Identify the blood parasite species.
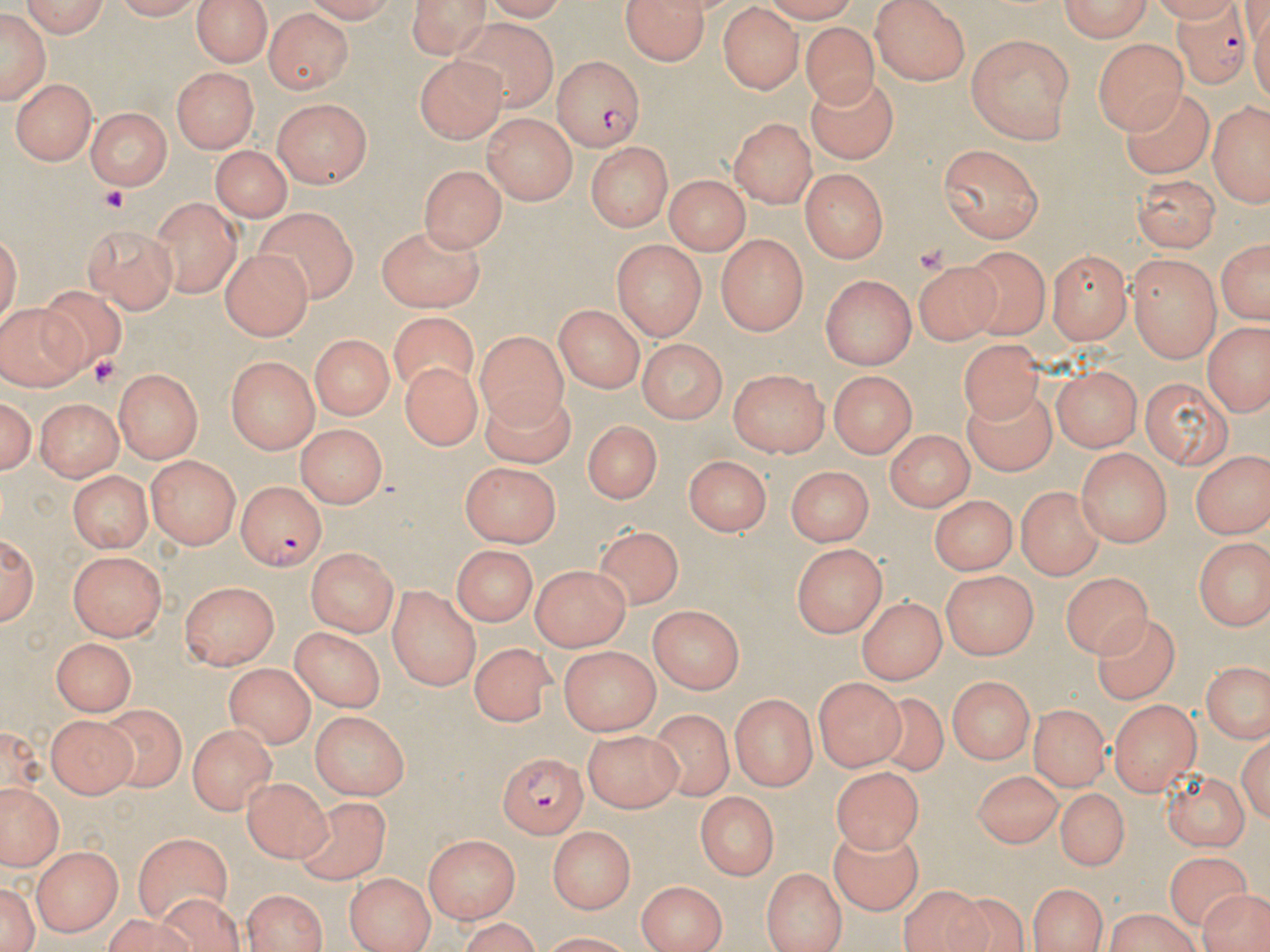
Plasmodium falciparum.

Approximate bounding boxes as (x1,y1)-(x2,y2) corner pairs in pixels. Platelet locations: (99,188)-(128,213), (86,355)-(122,389). Plasmodium falciparum-infected red blood cell locations: (1171,0)-(1251,91), (552,56)-(644,153), (233,480)-(324,569), (493,751)-(591,838). Uninfected red blood cell locations: (17,0)-(113,36), (105,0)-(200,21), (191,0)-(274,66), (403,0)-(494,56), (619,0)-(711,62), (1052,0)-(1152,40), (869,1)-(975,84), (0,6)-(46,107), (263,7)-(351,92), (717,8)-(801,94), (445,20)-(558,114), (802,22)-(877,106), (967,34)-(1076,144), (1093,37)-(1185,131), (417,56)-(507,143), (168,65)-(261,152), (807,76)-(896,164), (14,78)-(97,163), (1119,88)-(1214,180), (269,97)-(373,185), (1207,99)-(1270,207), (85,108)-(171,191), (481,112)-(578,203), (728,117)-(817,207), (587,141)-(674,230), (939,144)-(1045,244), (212,145)-(292,221), (420,164)-(508,255), (800,169)-(887,262), (1133,174)-(1220,254), (663,175)-(747,254), (150,196)-(243,296), (253,208)-(358,299), (1,221)-(22,334), (82,222)-(180,312), (374,223)-(488,310), (716,234)-(806,334), (1214,234)-(1268,330), (613,241)-(703,339), (963,243)-(1050,344), (1050,249)-(1130,346), (221,251)-(311,341), (1127,257)-(1222,364), (911,258)-(1001,343), (821,276)-(916,369), (34,288)-(127,371), (1,301)-(85,390), (555,303)-(647,393), (390,310)-(476,391), (1204,321)-(1269,417), (479,328)-(569,423), (308,335)-(391,421), (636,339)-(731,421), (960,342)-(1042,429), (227,358)-(321,452), (399,361)-(485,451), (730,366)-(831,455), (1052,366)-(1143,450), (114,368)-(204,462), (831,371)-(917,458), (1142,373)-(1234,466), (478,386)-(577,467), (959,386)-(1059,480), (0,390)-(38,483), (37,398)-(121,481), (579,422)-(662,507), (298,424)-(388,505), (885,429)-(971,513), (1076,447)-(1170,546), (1188,449)-(1269,540), (145,453)-(242,549), (687,453)-(774,535), (458,462)-(560,549), (785,464)-(873,547), (70,468)-(151,554), (1016,484)-(1105,579), (930,493)-(1014,573), (591,518)-(684,601), (2,529)-(38,630), (1195,535)-(1269,632), (791,543)-(882,636), (452,545)-(538,626), (306,548)-(397,636), (67,550)-(166,639), (529,564)-(628,648), (1061,567)-(1146,659), (941,572)-(1036,660), (177,580)-(276,668), (386,584)-(482,689), (858,594)-(944,684), (650,605)-(745,693), (1095,614)-(1177,707), (291,624)-(386,713), (51,638)-(132,715), (467,642)-(556,724), (559,647)-(657,736), (1202,664)-(1266,744), (227,667)-(314,745), (814,674)-(907,770), (945,674)-(1033,765), (871,692)-(950,776), (731,693)-(814,792), (1106,699)-(1198,794), (1028,704)-(1112,789), (100,705)-(185,790), (309,710)-(408,802), (646,711)-(738,806), (45,713)-(134,800), (190,725)-(276,816), (583,732)-(684,808), (973,764)-(1066,849), (1159,766)-(1247,851), (833,767)-(924,852), (237,775)-(338,863), (0,780)-(64,872), (1057,788)-(1126,869), (697,792)-(776,883), (296,798)-(386,885), (132,827)-(230,921), (550,827)-(636,912), (828,829)-(922,918), (423,832)-(519,923), (32,845)-(122,934), (1165,855)-(1250,927), (761,867)-(845,952), (345,872)-(433,952), (1,877)-(37,952), (638,879)-(728,949), (1028,882)-(1107,952), (1200,887)-(1270,952), (899,888)-(998,952), (241,889)-(327,951), (942,892)-(1032,952), (152,893)-(243,952), (1100,909)-(1204,952), (449,920)-(549,950). Single field of view. 1000x magnification. Thin blood film. Optical microscopy. Image is 1270×952 pixels. May-Grünwald-Giemsa stain.